Comment on the morphology of the red blood cells.
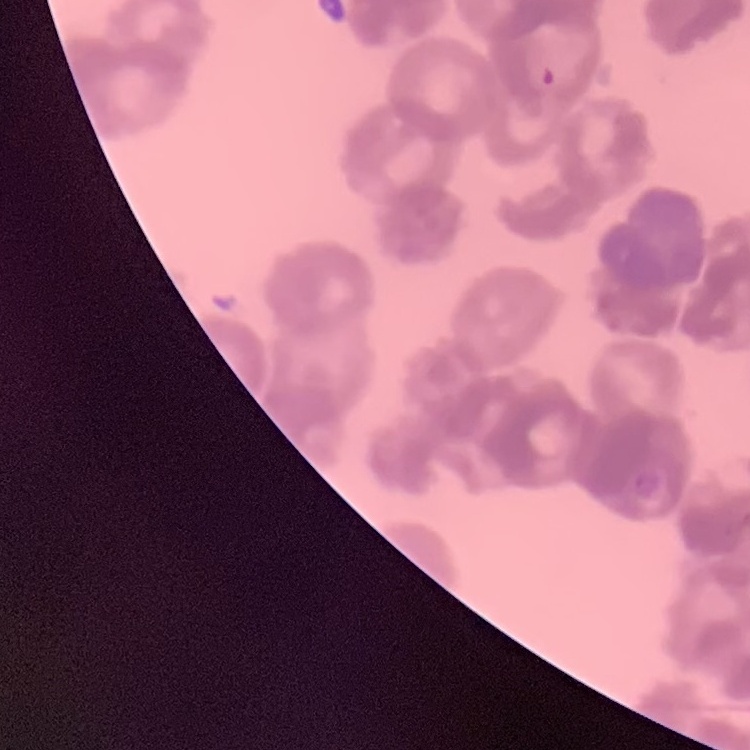

They show rouleaux formation.

Thin peripheral smear. Square crop of a larger photomicrograph. Field's or Giemsa stain.